Comment on the morphology of the red blood cells.
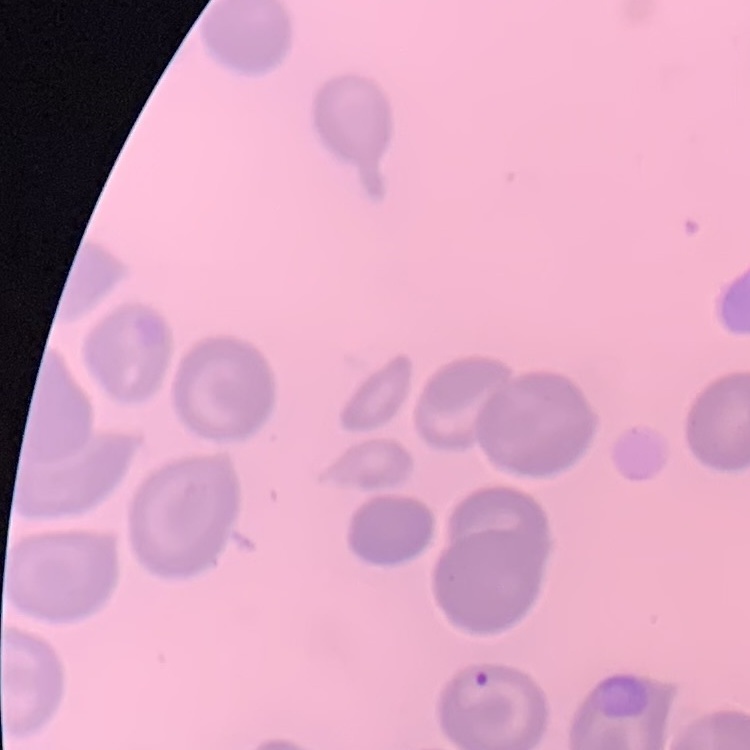
No rouleaux formation.

Summary:
  - Preparation: thin blood film
  - Image type: one tile cut from a larger photomicrograph
  - Stain: Field's or Giemsa